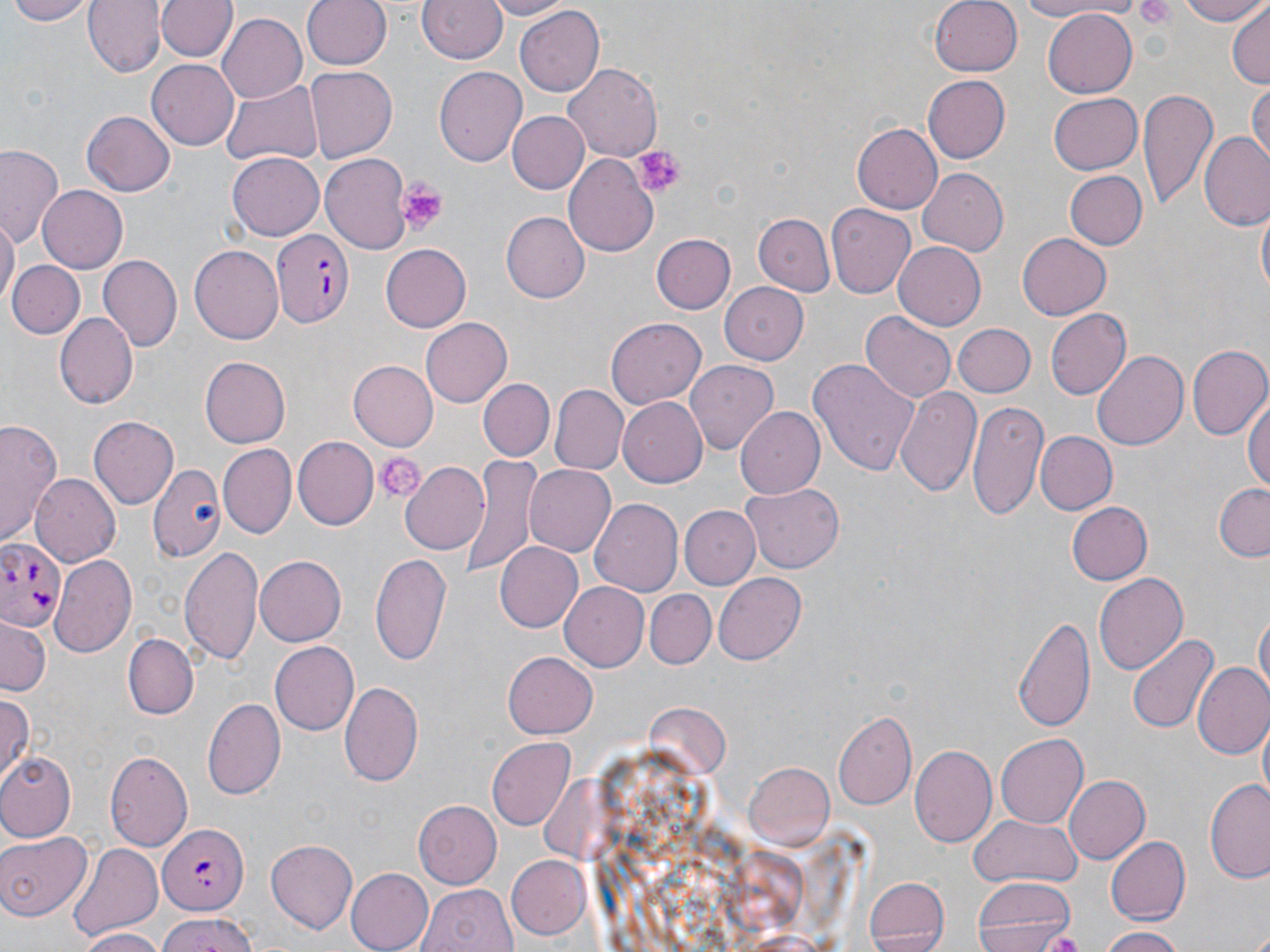

Approximate bounding boxes as named x1/y1/x2/y2 corners in pixels. Plasmodium falciparum-infected red blood cell locations: (x1=274, y1=229, x2=354, y2=330), (x1=1, y1=539, x2=69, y2=635), (x1=154, y1=826, x2=246, y2=916). Uninfected red blood cell locations: (x1=7, y1=0, x2=94, y2=24), (x1=82, y1=0, x2=163, y2=78), (x1=156, y1=0, x2=238, y2=64), (x1=299, y1=0, x2=390, y2=71), (x1=481, y1=0, x2=578, y2=19), (x1=930, y1=0, x2=1024, y2=75), (x1=1012, y1=0, x2=1127, y2=20), (x1=1179, y1=0, x2=1267, y2=25), (x1=418, y1=1, x2=507, y2=65), (x1=1227, y1=4, x2=1269, y2=88), (x1=516, y1=6, x2=605, y2=95), (x1=1042, y1=7, x2=1136, y2=96), (x1=217, y1=14, x2=307, y2=104), (x1=147, y1=59, x2=240, y2=151), (x1=563, y1=60, x2=661, y2=158), (x1=435, y1=66, x2=525, y2=168), (x1=305, y1=67, x2=397, y2=161), (x1=920, y1=74, x2=1009, y2=164), (x1=1250, y1=80, x2=1269, y2=169), (x1=221, y1=81, x2=321, y2=167), (x1=1137, y1=88, x2=1215, y2=211), (x1=1049, y1=93, x2=1144, y2=173), (x1=81, y1=110, x2=174, y2=197), (x1=505, y1=110, x2=589, y2=195), (x1=851, y1=121, x2=942, y2=215), (x1=1199, y1=132, x2=1270, y2=230), (x1=1, y1=144, x2=65, y2=245), (x1=322, y1=153, x2=414, y2=253), (x1=562, y1=153, x2=661, y2=257), (x1=228, y1=155, x2=323, y2=241), (x1=916, y1=167, x2=1007, y2=256), (x1=1065, y1=170, x2=1146, y2=249), (x1=38, y1=186, x2=128, y2=273), (x1=827, y1=204, x2=915, y2=297), (x1=1256, y1=205, x2=1269, y2=302), (x1=751, y1=211, x2=834, y2=297), (x1=502, y1=212, x2=589, y2=302), (x1=0, y1=218, x2=18, y2=311), (x1=1016, y1=231, x2=1111, y2=320), (x1=652, y1=233, x2=735, y2=314), (x1=894, y1=242, x2=987, y2=330), (x1=190, y1=244, x2=285, y2=344), (x1=381, y1=244, x2=470, y2=332), (x1=98, y1=255, x2=180, y2=350), (x1=7, y1=259, x2=83, y2=338), (x1=720, y1=280, x2=811, y2=363), (x1=1045, y1=309, x2=1132, y2=398), (x1=861, y1=312, x2=955, y2=402), (x1=57, y1=313, x2=140, y2=406), (x1=420, y1=317, x2=513, y2=408), (x1=607, y1=320, x2=705, y2=409), (x1=951, y1=323, x2=1035, y2=397), (x1=1187, y1=344, x2=1270, y2=441), (x1=1092, y1=350, x2=1190, y2=450), (x1=200, y1=355, x2=291, y2=448), (x1=810, y1=358, x2=920, y2=476), (x1=346, y1=360, x2=437, y2=450), (x1=685, y1=361, x2=778, y2=455), (x1=477, y1=377, x2=554, y2=461), (x1=894, y1=382, x2=982, y2=496), (x1=551, y1=386, x2=626, y2=473), (x1=1247, y1=392, x2=1269, y2=496), (x1=617, y1=397, x2=706, y2=487), (x1=969, y1=399, x2=1049, y2=520), (x1=738, y1=406, x2=826, y2=499), (x1=89, y1=415, x2=178, y2=508), (x1=0, y1=418, x2=64, y2=549), (x1=1034, y1=431, x2=1115, y2=516), (x1=295, y1=436, x2=379, y2=528), (x1=220, y1=444, x2=295, y2=535), (x1=458, y1=455, x2=542, y2=575), (x1=400, y1=461, x2=492, y2=553), (x1=522, y1=463, x2=616, y2=557), (x1=148, y1=465, x2=226, y2=562), (x1=31, y1=474, x2=120, y2=567), (x1=741, y1=483, x2=846, y2=574), (x1=1213, y1=483, x2=1270, y2=561), (x1=591, y1=498, x2=686, y2=595), (x1=1066, y1=501, x2=1152, y2=585), (x1=681, y1=504, x2=759, y2=587), (x1=496, y1=543, x2=582, y2=631), (x1=180, y1=544, x2=265, y2=665), (x1=369, y1=551, x2=452, y2=665), (x1=50, y1=554, x2=136, y2=655), (x1=255, y1=555, x2=346, y2=647), (x1=1093, y1=571, x2=1188, y2=676), (x1=713, y1=572, x2=808, y2=663), (x1=562, y1=580, x2=652, y2=670), (x1=644, y1=590, x2=714, y2=669), (x1=1254, y1=608, x2=1269, y2=698), (x1=1013, y1=612, x2=1096, y2=734), (x1=0, y1=620, x2=49, y2=695), (x1=125, y1=633, x2=199, y2=719), (x1=1127, y1=633, x2=1220, y2=735), (x1=269, y1=640, x2=361, y2=736), (x1=502, y1=653, x2=596, y2=739), (x1=1193, y1=662, x2=1270, y2=760), (x1=337, y1=681, x2=425, y2=788), (x1=0, y1=692, x2=33, y2=784), (x1=203, y1=697, x2=287, y2=800), (x1=835, y1=710, x2=917, y2=809), (x1=1257, y1=720, x2=1270, y2=804), (x1=995, y1=732, x2=1088, y2=828), (x1=486, y1=737, x2=576, y2=832), (x1=910, y1=744, x2=997, y2=847), (x1=105, y1=749, x2=193, y2=854), (x1=0, y1=752, x2=76, y2=840), (x1=742, y1=763, x2=834, y2=851), (x1=1063, y1=775, x2=1149, y2=866), (x1=1205, y1=780, x2=1270, y2=883), (x1=414, y1=801, x2=502, y2=887), (x1=968, y1=812, x2=1081, y2=888), (x1=0, y1=829, x2=89, y2=920), (x1=1105, y1=836, x2=1190, y2=925), (x1=264, y1=837, x2=356, y2=931), (x1=68, y1=841, x2=164, y2=941), (x1=504, y1=854, x2=593, y2=939), (x1=344, y1=867, x2=433, y2=952), (x1=973, y1=876, x2=1077, y2=952), (x1=863, y1=877, x2=948, y2=952), (x1=417, y1=883, x2=517, y2=952), (x1=153, y1=916, x2=259, y2=952), (x1=1096, y1=926, x2=1183, y2=952), (x1=73, y1=929, x2=169, y2=952), (x1=1036, y1=930, x2=1088, y2=948). Platelet locations: (x1=633, y1=145, x2=684, y2=198), (x1=396, y1=177, x2=450, y2=233), (x1=376, y1=450, x2=426, y2=502). Slide-level diagnosis: Plasmodium falciparum. Thin blood film. Optical microscopy. Image is 1270×952 pixels. May-Grünwald-Giemsa stain. Single field of view. 1000x magnification.